Identify the parasite.
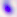
This is Toxoplasma gondii.

Summary:
  - Modality: micrograph
  - Magnification: 400x